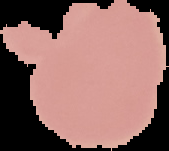
Summary:
  - Image type: segmented cell region with the area outside set to black
  - Malaria status: uninfected
  - Preparation: thin blood film
  - Image size: 169×151 pixels